Locate every Plasmodium parasite.
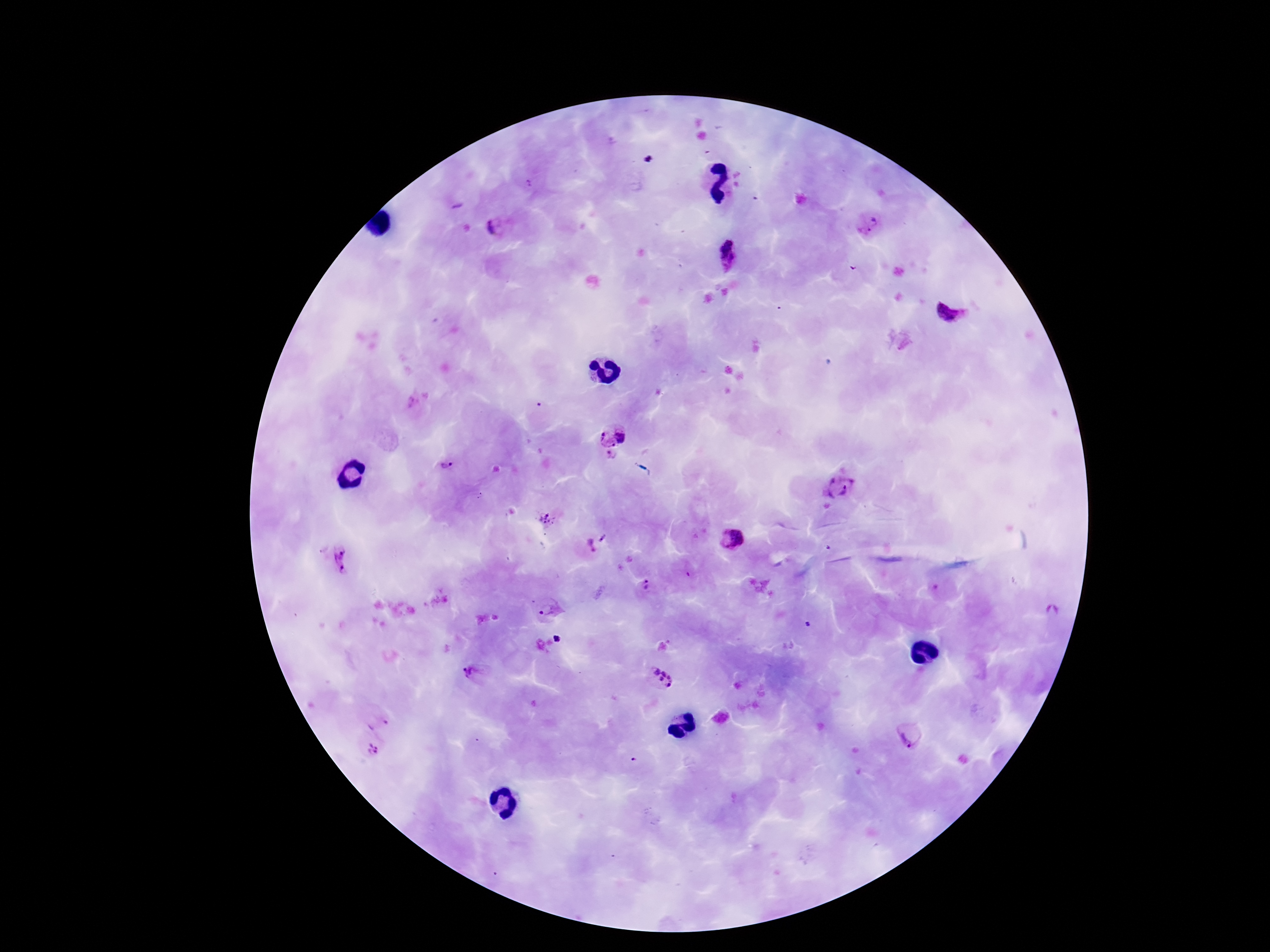
Approximate centers as (x, y) in pixels.
Plasmodium parasites: (870, 224), (497, 225), (727, 256), (950, 311), (610, 433), (611, 455), (445, 465), (837, 487), (481, 496), (548, 517), (733, 540), (588, 547), (343, 560), (648, 587), (550, 609), (557, 639), (475, 673), (659, 678), (911, 734), (371, 748).

Summary:
  - Stain: Giemsa
  - Patient malaria status: infected
  - Preparation: thick peripheral-blood smear
  - Magnification: 100x
  - Image size: 1270×952 pixels
  - Field of view: one from this slide
  - Capture: smartphone camera through the microscope eyepiece